Describe the morphology of the red blood cells.
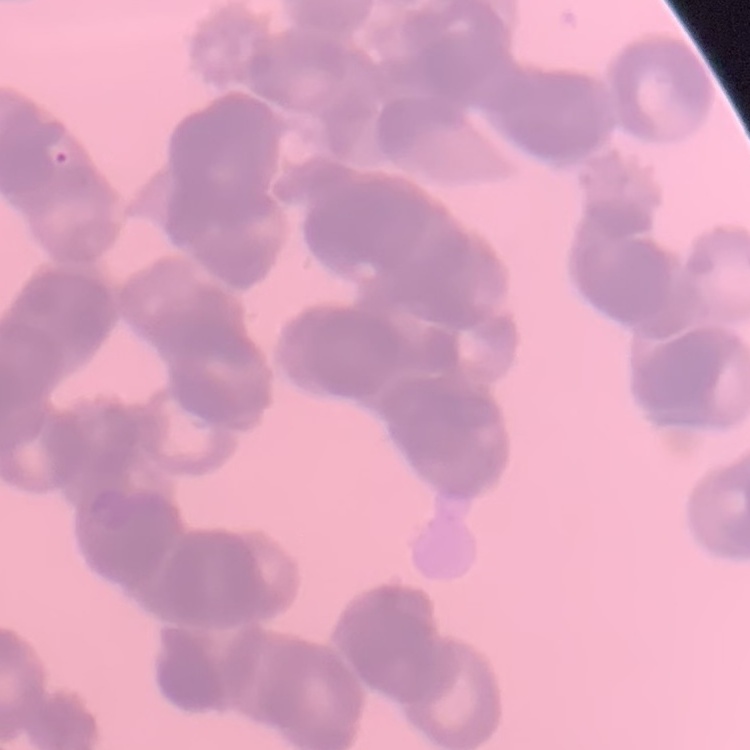
They show rouleaux formation.

preparation = thin peripheral smear
stain = Field's or Giemsa
image type = square crop of a larger photomicrograph